Assess for Plasmodium parasites.
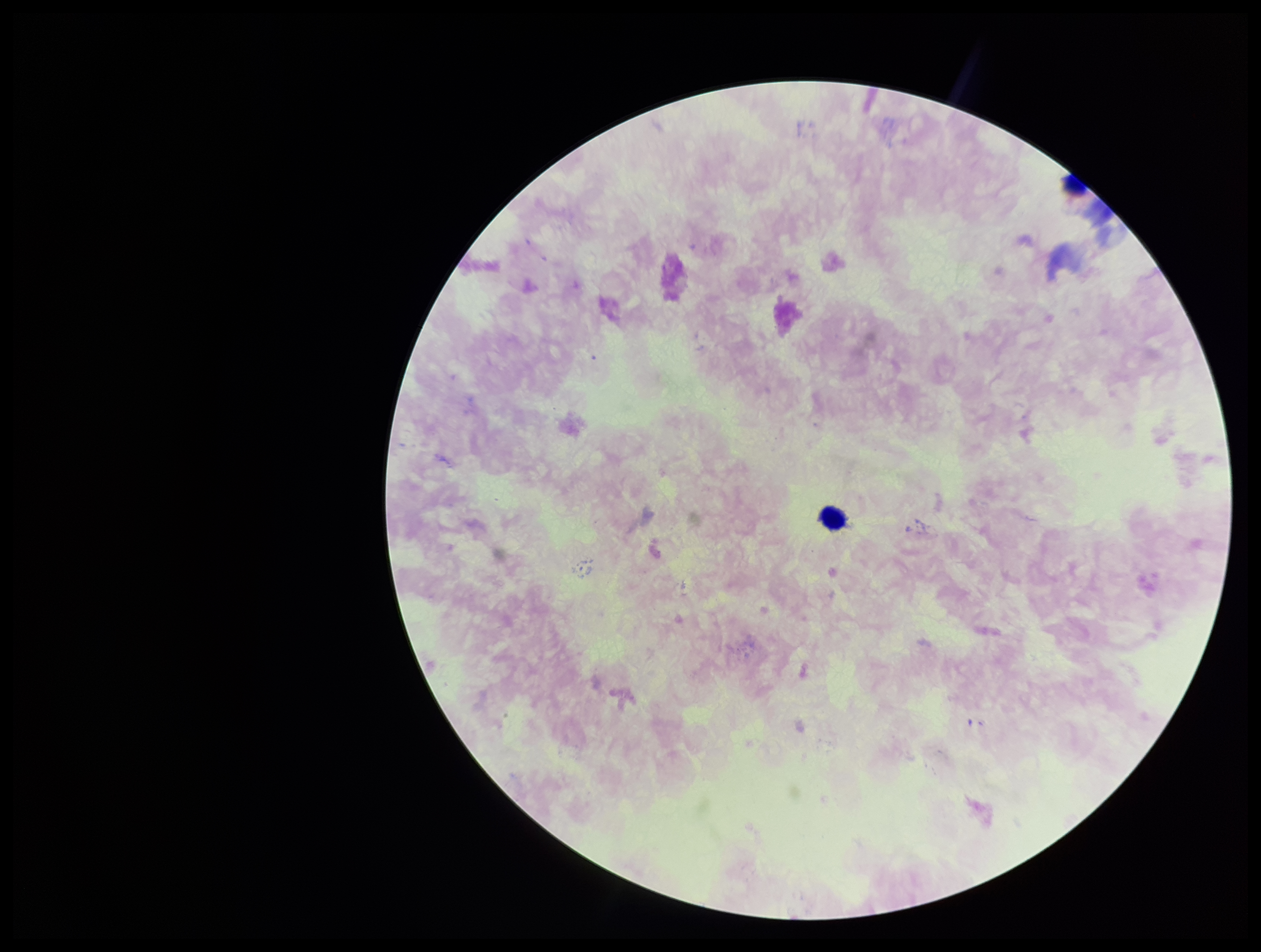

None detected.

Patient malaria status: negative. Smartphone photograph taken through the eyepiece of a microscope. Parasite count: 0. Image is 1261×952 pixels. Single field of view. Preparation: thick blood smear. Giemsa stain. Leukocyte count: 1.